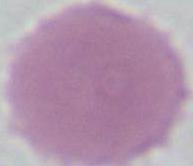
Summary:
  - Magnification: 1000x
  - Modality: micrograph
  - Identification: erythrocyte